Classify this cell by malaria status.
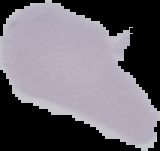
Uninfected.

{
  "preparation": "thin blood film",
  "image_type": "segmented cell region with the area outside set to black",
  "image_size": "160×151 pixels"
}